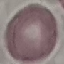

Summary:
  - Result: negative for malaria parasites
  - Stain: Giemsa
  - Image type: automatically extracted cell patch, resized to 64 × 64 pixels
  - Capture: smartphone camera at the microscope eyepiece
  - Preparation: thin blood smear